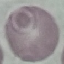
malaria status = uninfected
preparation = thin blood film
image type = automatically extracted cell patch, resized to 64 × 64 pixels
capture = smartphone camera at the microscope eyepiece
stain = Giemsa